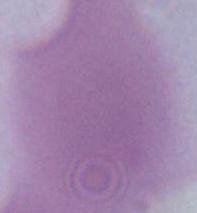
magnification: 1000x
identification: red blood cell
modality: micrograph